Locate and identify every blood parasite.
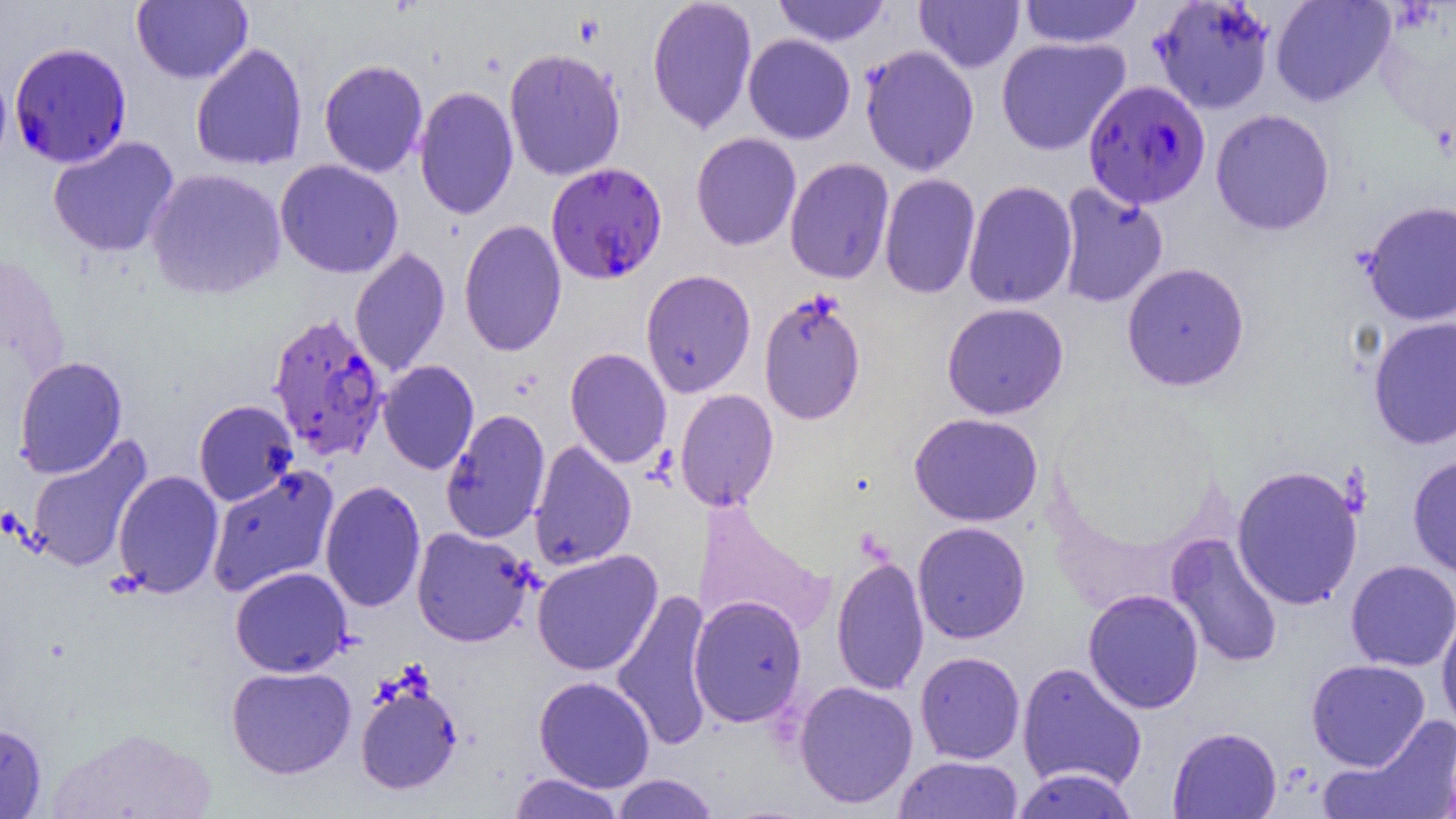
Approximate bounding boxes as (x1,y1)-(x2,y2) corner pairs in pixels.
Plasmodium falciparum-infected red blood cells: (9,41)-(132,169), (1083,79)-(1211,210), (545,161)-(668,285), (268,312)-(389,463).
No Plasmodium ovale, Plasmodium malariae, Plasmodium vivax, Babesia divergens, or Trypanosoma brucei observed.

Uninfected red blood cell locations: (131,0)-(253,84), (647,0)-(758,134), (771,0)-(892,47), (914,0)-(1025,73), (1017,0)-(1144,49), (1149,1)-(1277,115), (1270,1)-(1397,108), (1373,4)-(1455,147), (742,33)-(856,145), (996,36)-(1130,155), (190,42)-(309,171), (859,45)-(980,176), (504,47)-(626,182), (319,58)-(429,178), (413,85)-(519,220), (1210,108)-(1335,236), (691,132)-(802,251), (47,135)-(180,258), (784,157)-(895,284), (275,159)-(404,279), (146,168)-(287,301), (879,172)-(981,299), (963,180)-(1078,310), (1055,182)-(1169,309), (1360,199)-(1456,326), (458,219)-(567,357), (349,247)-(451,377), (1121,262)-(1250,392), (640,268)-(757,398), (758,290)-(866,425), (941,302)-(1069,420), (1367,316)-(1456,450), (564,347)-(672,469), (13,355)-(127,479), (378,360)-(479,475), (675,388)-(779,511), (193,400)-(299,507), (440,408)-(551,544), (909,412)-(1043,527), (25,435)-(153,573), (528,440)-(637,571), (1407,454)-(1456,579), (206,464)-(340,598), (1231,464)-(1364,610), (113,470)-(224,598), (320,480)-(426,612), (913,521)-(1031,644), (412,527)-(535,647), (1165,532)-(1284,669), (531,549)-(663,677), (831,553)-(929,696), (1345,559)-(1456,672), (230,566)-(352,677), (611,588)-(715,751), (1083,588)-(1204,714), (688,595)-(808,728), (1436,608)-(1456,735), (915,651)-(1025,764), (1306,658)-(1430,770), (1017,662)-(1147,792), (226,665)-(356,779), (533,676)-(655,792), (794,680)-(919,808), (355,682)-(462,794), (1322,715)-(1456,819), (0,724)-(46,818), (1168,726)-(1282,818), (894,755)-(1024,818), (1011,767)-(1140,819), (508,773)-(625,819), (611,774)-(718,818). Slide-level diagnosis: Plasmodium falciparum. Thin blood film. Light microscopy. Captured at 1000x magnification. Image is 1456×819 pixels. Single field of view.